Outline each Plasmodium falciparum parasite and classify it by life-cycle stage.
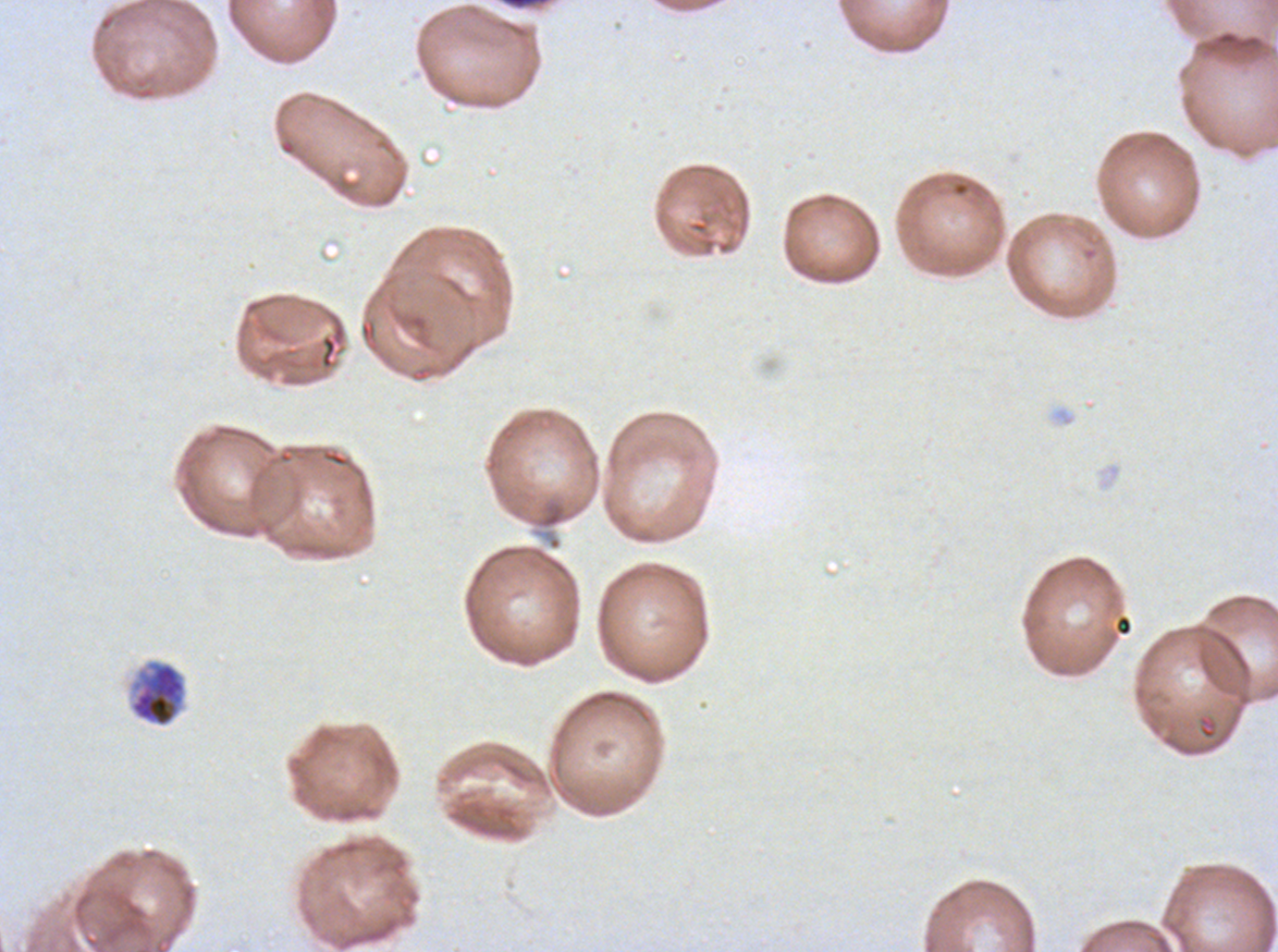

Approximate bounding boxes as (x1, y1, x2, y2) in pixels.
Early schizonts: (129, 660, 187, 727).
No rings, late-ring/early-trophozoite forms, mid trophozoites, late trophozoites, late schizonts, segmenters, or gametocytes observed.

Plasmodium falciparum from a patient in The Gambia, cultured ex vivo for 24 to 48 hours. Thin blood film. One sub-image of a larger composite. Giemsa-stained preparation. Image is 1278×952 pixels.